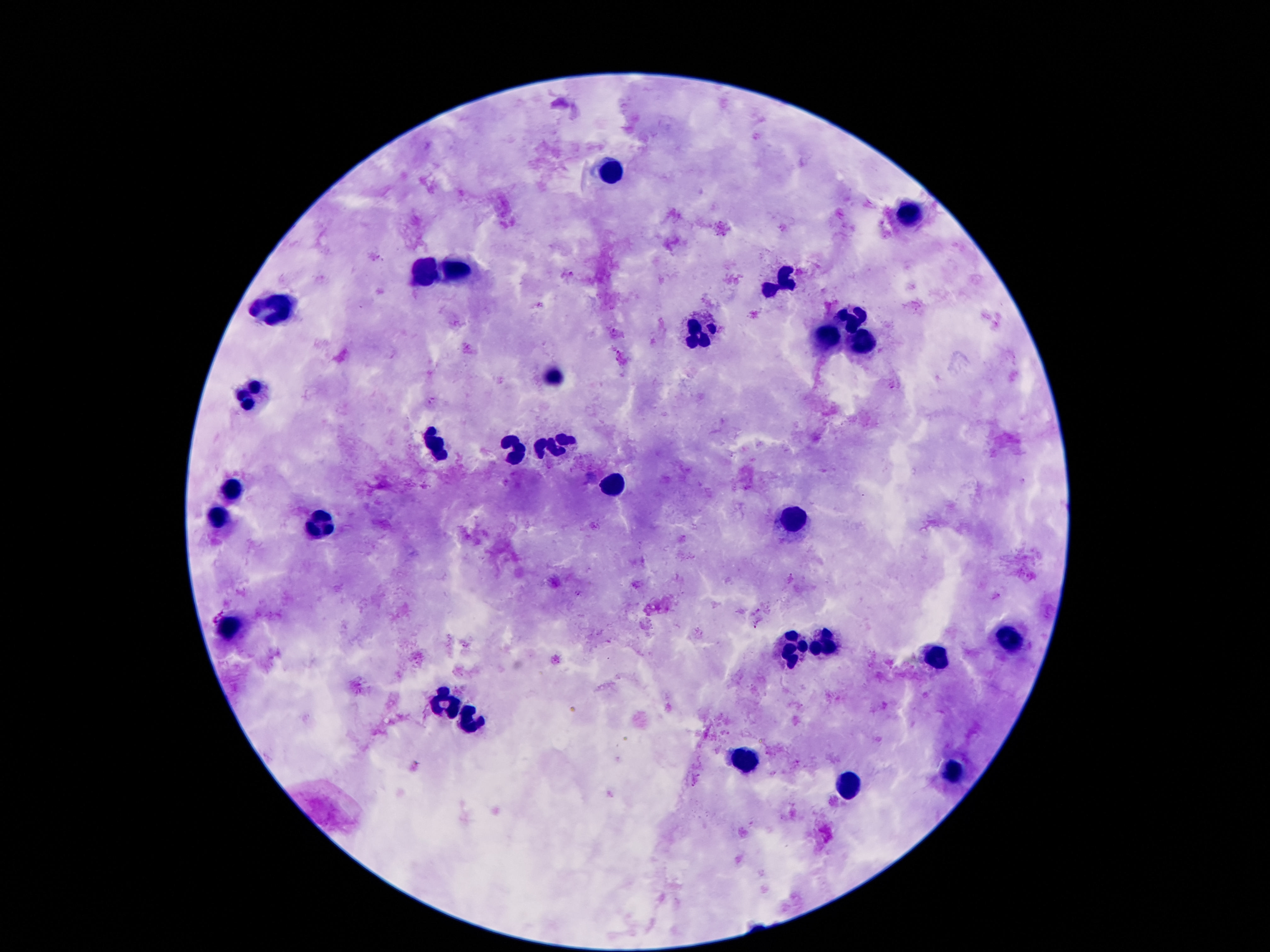

leukocyte locations = approximate centers as {x, y} in pixels: {612, 171}, {910, 216}, {427, 272}, {458, 273}, {782, 283}, {276, 306}, {851, 316}, {700, 335}, {830, 338}, {862, 344}, {555, 369}, {253, 394}, {515, 448}, {555, 448}, {437, 449}, {614, 483}, {230, 491}, {219, 520}, {792, 522}, {326, 527}, {227, 628}, {1009, 639}, {824, 640}, {794, 650}, {937, 658}, {448, 703}, {471, 722}, {744, 762}, {952, 770}, {847, 788}
capture = smartphone camera through the microscope eyepiece
field of view = single
preparation = thick blood film
patient malaria status = uninfected
stain = Giemsa
image size = 1270×952 pixels
magnification = 100x